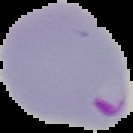
malaria status = parasitized
preparation = thin blood film
image size = 133×133 pixels
image type = cell region segmented out of the field of view; surrounding area masked to black